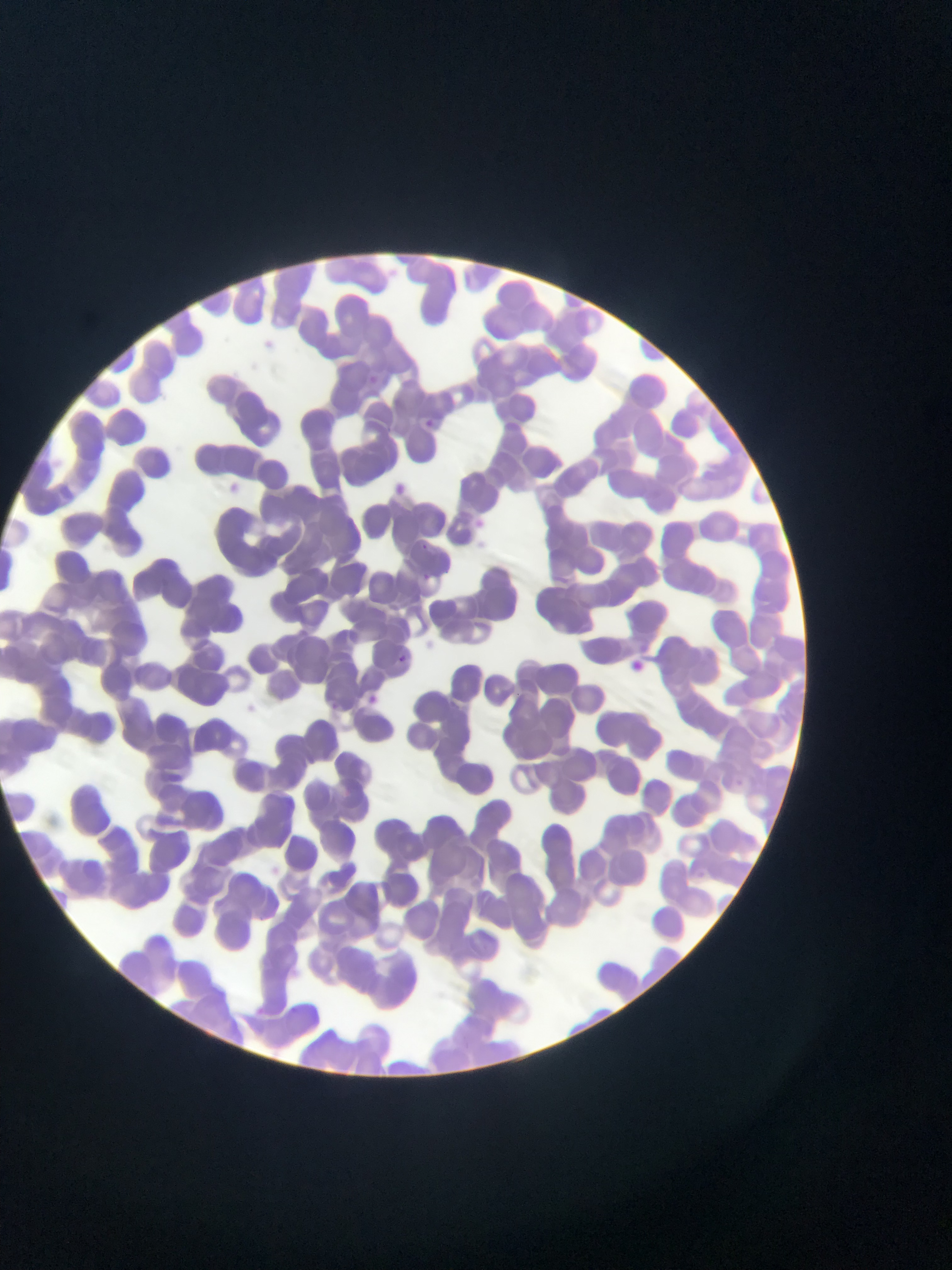
Approximate bounding boxes as (left, top, right, bottom) in pixels.
Summary:
  - Plasmodium parasite locations: (425, 416, 438, 429), (420, 540, 430, 555), (423, 572, 434, 584), (397, 653, 408, 670), (328, 699, 340, 711), (729, 773, 742, 782)
  - Country: Ghana
  - Preparation: thin blood smear
  - Image size: 952×1270 pixels
  - Field of view: single
  - Capture: mobile-phone photograph through a microscope